Assess this cell for malaria.
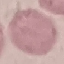
It is uninfected.

Giemsa-stained preparation. Cell patch, automatically extracted from a larger field of view and resized to 64 × 64 pixels. Acquired by smartphone through the microscope eyepiece. Thin blood smear.